Identify the preparation type.
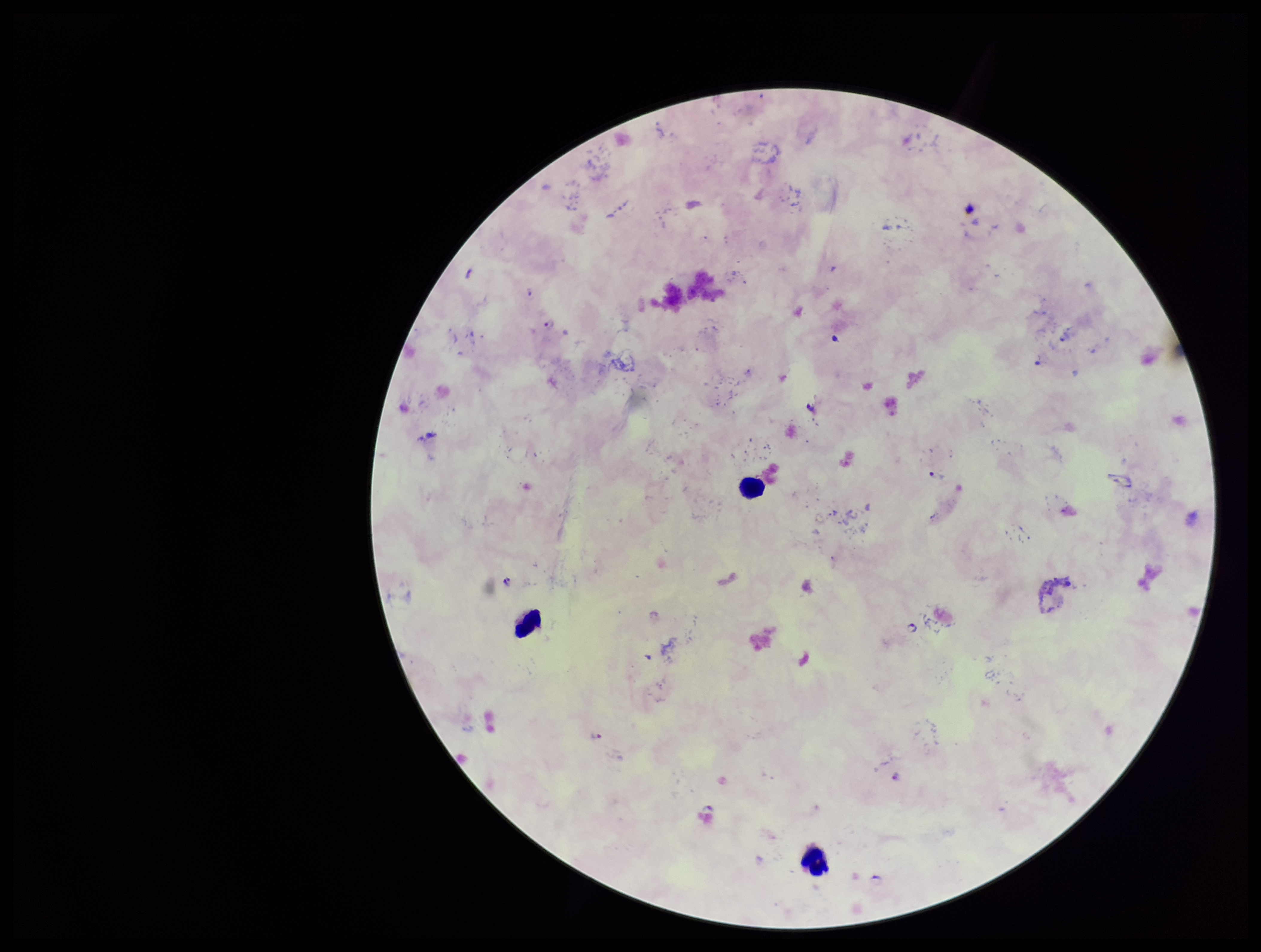
A thick smear.

Stained with Giemsa. Photographed through the microscope eyepiece with a smartphone camera. Image is 1261×952 pixels. Leukocyte count: 3. Patient malaria status: positive. Single field of view. Parasite count: 4. Plasmodium parasites: detected. Species reported for this patient: Plasmodium falciparum.